Name the blood parasite species.
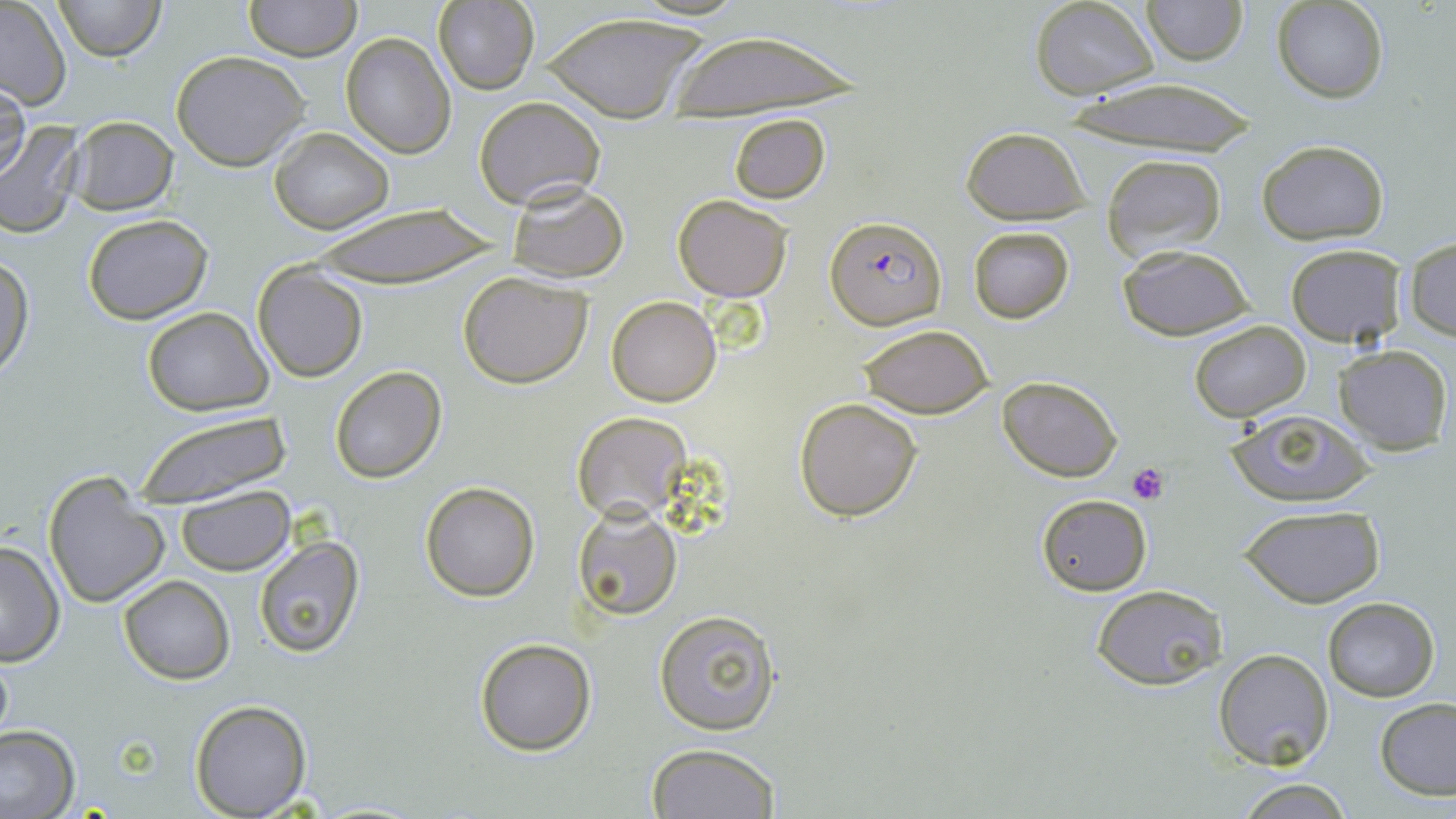

Plasmodium falciparum.

Summary:
  - Coordinate format: approximate bounding boxes as (x1, y1, x2, y2) in pixels
  - Platelet locations: (1128, 462, 1169, 505)
  - Uninfected red blood cell locations: (54, 0, 165, 61), (243, 0, 360, 62), (1142, 0, 1248, 65), (434, 1, 537, 93), (1030, 1, 1161, 99), (1272, 1, 1390, 102), (0, 4, 73, 109), (536, 11, 710, 122), (664, 30, 866, 120), (340, 31, 455, 158), (171, 51, 311, 171), (0, 77, 28, 185), (1064, 80, 1259, 155), (474, 95, 605, 208), (729, 112, 830, 202), (68, 116, 178, 215), (0, 122, 84, 238), (269, 126, 393, 234), (958, 126, 1093, 224), (1256, 139, 1390, 244), (1101, 153, 1229, 261), (505, 182, 630, 283), (672, 194, 793, 302), (308, 202, 496, 290), (81, 212, 213, 325), (968, 226, 1076, 324), (1404, 236, 1456, 340), (1284, 243, 1407, 348), (1114, 244, 1256, 340), (1, 253, 34, 379), (252, 263, 368, 382), (458, 272, 594, 388), (605, 295, 722, 406), (140, 307, 274, 415), (1189, 321, 1310, 421), (857, 325, 995, 418), (1332, 345, 1451, 454), (328, 364, 446, 483), (998, 374, 1122, 481), (793, 397, 923, 521), (135, 408, 291, 508), (1224, 409, 1375, 507), (571, 412, 691, 522), (43, 471, 170, 611), (420, 482, 539, 601), (175, 486, 293, 575), (1036, 494, 1152, 595), (572, 504, 683, 621), (1239, 504, 1386, 608), (252, 536, 366, 659), (0, 540, 63, 668), (118, 576, 234, 684), (1090, 583, 1231, 693), (1321, 597, 1440, 701), (653, 609, 779, 735), (475, 638, 596, 756), (1214, 648, 1334, 770), (0, 649, 14, 751), (1375, 697, 1456, 800), (188, 699, 312, 817), (1, 727, 78, 816), (647, 744, 781, 819), (1235, 779, 1355, 817)
  - Plasmodium falciparum-infected red blood cell locations: (826, 215, 945, 331)
  - Preparation: thin blood film
  - Field of view: one of a larger specimen
  - Stain: May-Grünwald-Giemsa
  - Magnification: 1000x
  - Modality: light microscopy
  - Image size: 1456×819 pixels